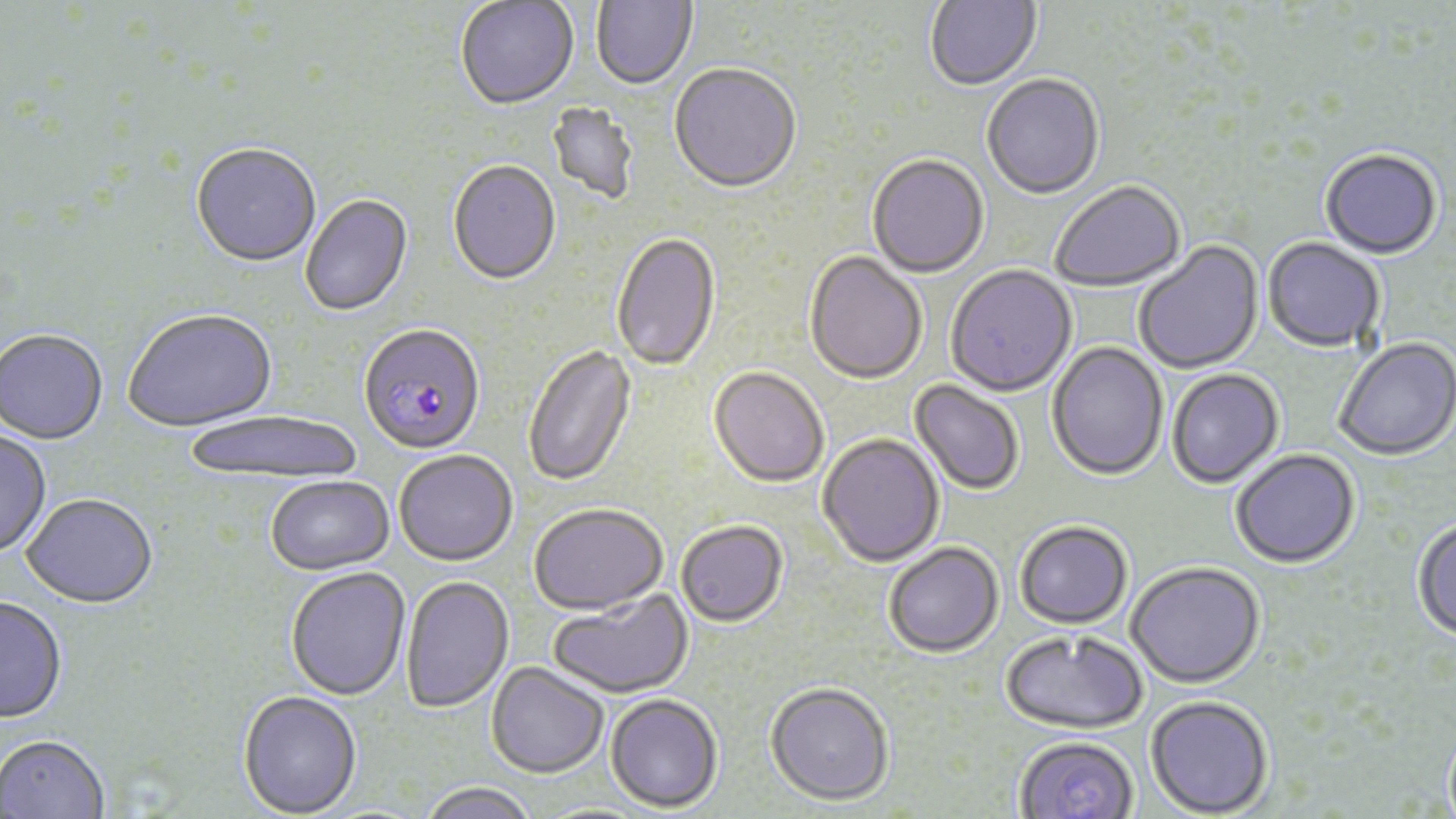
slide-level diagnosis = Plasmodium falciparum
stain = May-Grünwald-Giemsa
modality = light microscopy
magnification = 1000x
field of view = single
image size = 1456×819 pixels
preparation = thin blood smear
uninfected red blood cell locations = approximate bounding boxes as named x1/y1/x2/y2 corners in pixels: (x1=925, y1=0, x2=1042, y2=92), (x1=455, y1=1, x2=579, y2=112), (x1=591, y1=1, x2=698, y2=91), (x1=668, y1=65, x2=802, y2=197), (x1=982, y1=75, x2=1105, y2=201), (x1=546, y1=101, x2=640, y2=207), (x1=190, y1=145, x2=321, y2=269), (x1=1320, y1=151, x2=1443, y2=261), (x1=867, y1=156, x2=989, y2=279), (x1=447, y1=162, x2=561, y2=288), (x1=1051, y1=182, x2=1187, y2=294), (x1=301, y1=195, x2=414, y2=318), (x1=611, y1=233, x2=721, y2=373), (x1=1262, y1=239, x2=1385, y2=354), (x1=1135, y1=241, x2=1265, y2=376), (x1=804, y1=252, x2=927, y2=386), (x1=945, y1=266, x2=1077, y2=398), (x1=123, y1=310, x2=278, y2=435), (x1=0, y1=331, x2=108, y2=446), (x1=1334, y1=339, x2=1456, y2=462), (x1=1047, y1=342, x2=1168, y2=482), (x1=522, y1=345, x2=636, y2=488), (x1=708, y1=368, x2=829, y2=489), (x1=1167, y1=370, x2=1284, y2=490), (x1=909, y1=380, x2=1024, y2=496), (x1=184, y1=411, x2=365, y2=485), (x1=0, y1=430, x2=52, y2=559), (x1=816, y1=434, x2=945, y2=569), (x1=394, y1=450, x2=518, y2=566), (x1=1231, y1=450, x2=1361, y2=569), (x1=265, y1=476, x2=396, y2=576), (x1=21, y1=496, x2=158, y2=611), (x1=529, y1=503, x2=668, y2=616), (x1=1412, y1=518, x2=1456, y2=642), (x1=675, y1=521, x2=789, y2=628), (x1=1015, y1=522, x2=1133, y2=630), (x1=883, y1=543, x2=1005, y2=659), (x1=1126, y1=564, x2=1265, y2=690), (x1=285, y1=567, x2=411, y2=701), (x1=401, y1=576, x2=514, y2=714), (x1=548, y1=590, x2=694, y2=699), (x1=0, y1=598, x2=67, y2=724), (x1=1001, y1=631, x2=1148, y2=735), (x1=486, y1=662, x2=609, y2=778), (x1=764, y1=682, x2=894, y2=807), (x1=238, y1=691, x2=362, y2=818), (x1=604, y1=694, x2=723, y2=813), (x1=1144, y1=696, x2=1273, y2=817), (x1=0, y1=736, x2=110, y2=819), (x1=1013, y1=737, x2=1139, y2=819), (x1=417, y1=782, x2=539, y2=819)
Plasmodium falciparum-infected red blood cell locations = approximate bounding boxes as named x1/y1/x2/y2 corners in pixels: (x1=358, y1=326, x2=486, y2=456)